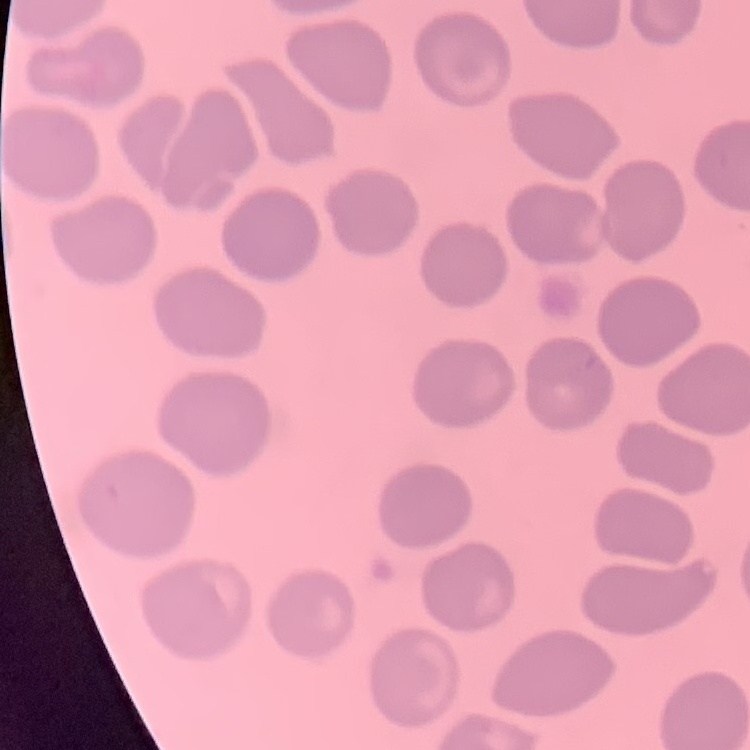

Summary:
  - Erythrocyte morphology: no rouleaux formation
  - Preparation: thin peripheral smear
  - Image type: one tile cut from a larger photomicrograph
  - Stain: Field's or Giemsa